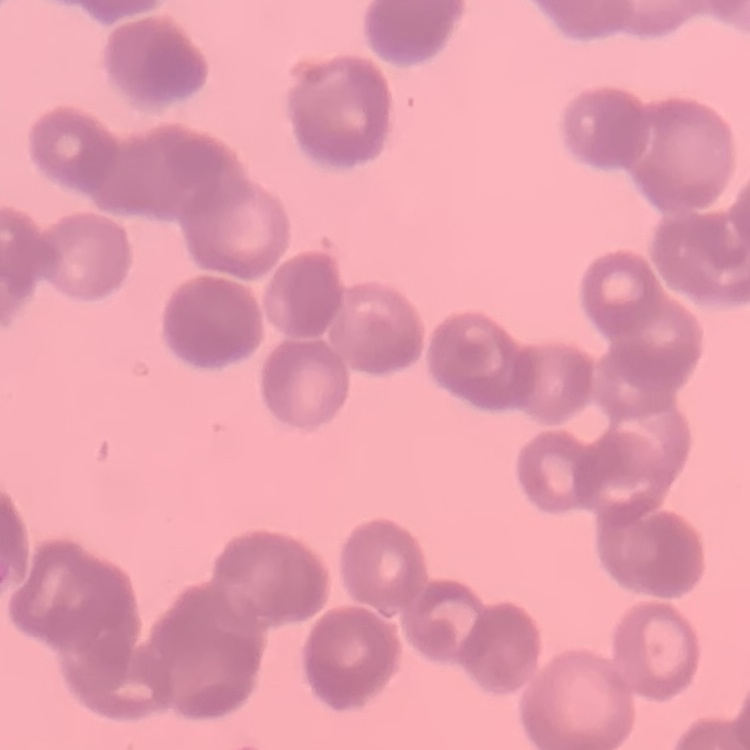

{
  "erythrocyte_morphology": "rouleaux formation",
  "preparation": "thin blood film",
  "image_type": "one tile cut from a larger photomicrograph",
  "stain": "Field's or Giemsa"
}